State which parasite is depicted.
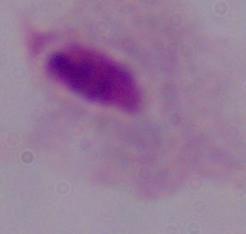
This is a trichomonad.

Summary:
  - Magnification: 1000x
  - Modality: photomicrograph